Comment on the morphology of the red blood cells.
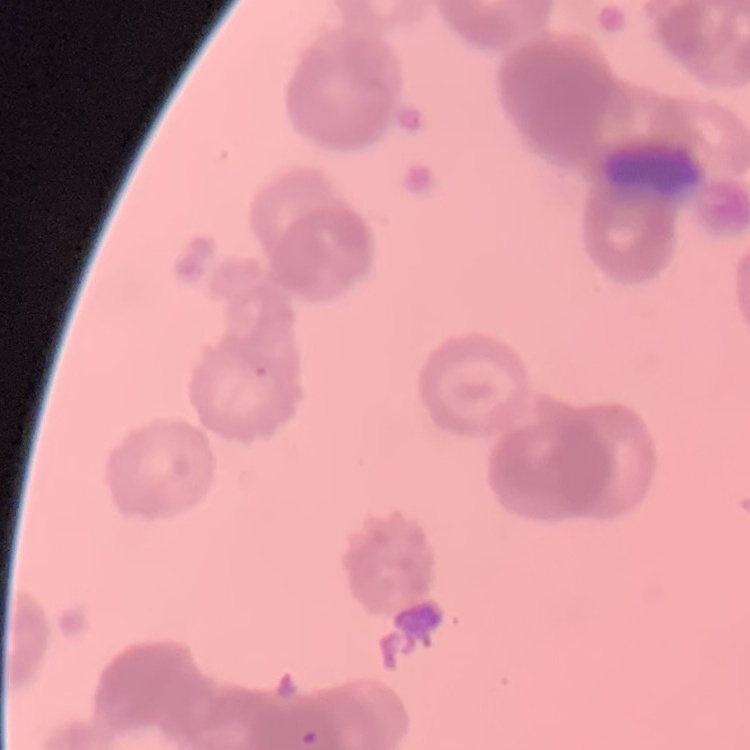
They show rouleaux formation.

Summary:
  - Stain: Field's or Giemsa
  - Image type: one tile cut from a larger photomicrograph
  - Preparation: thin peripheral smear